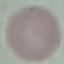

result = no malaria parasites seen
preparation = thin blood film
capture = smartphone camera at the microscope eyepiece
stain = Giemsa
image type = automatically extracted cell patch, resized to 64 × 64 pixels